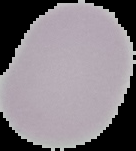

From a thin blood film. Malaria status: uninfected. Segmented cell region on a black background. Image is 136×151 pixels.